Assess the morphology of the erythrocytes.
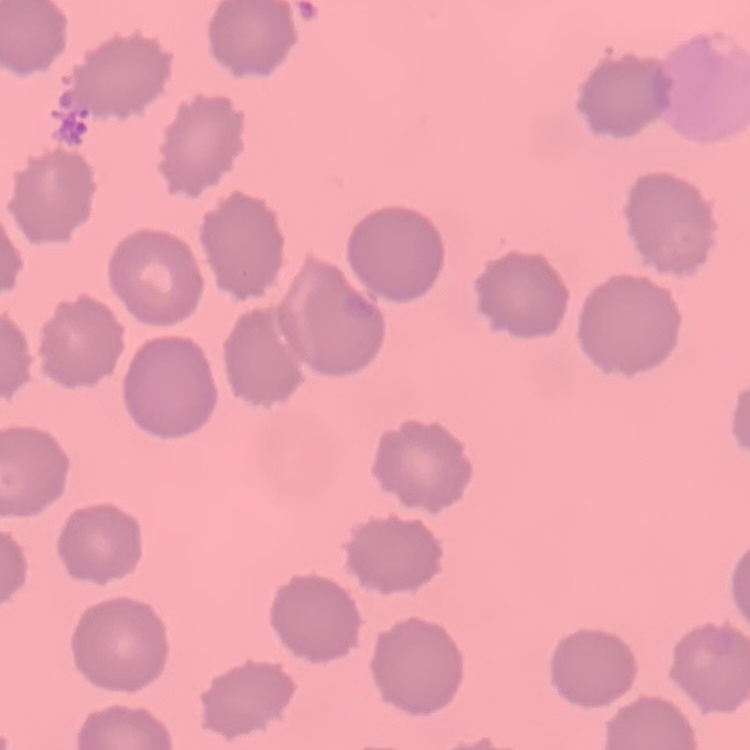
No rouleaux formation.

image type = square crop of a larger photomicrograph
preparation = thin peripheral smear
stain = Field's or Giemsa